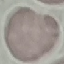

Summary:
  - Result: no malaria parasites detected
  - Preparation: thin blood smear
  - Capture: smartphone through the microscope eyepiece
  - Image type: automatically extracted cell patch, resized to 64 × 64 pixels
  - Stain: Giemsa